Report the malaria status of this cell.
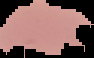

Uninfected.

Summary:
  - Preparation: thin blood smear
  - Image size: 94×58 pixels
  - Image type: segmented cell region on a black background